Point out each Plasmodium parasite.
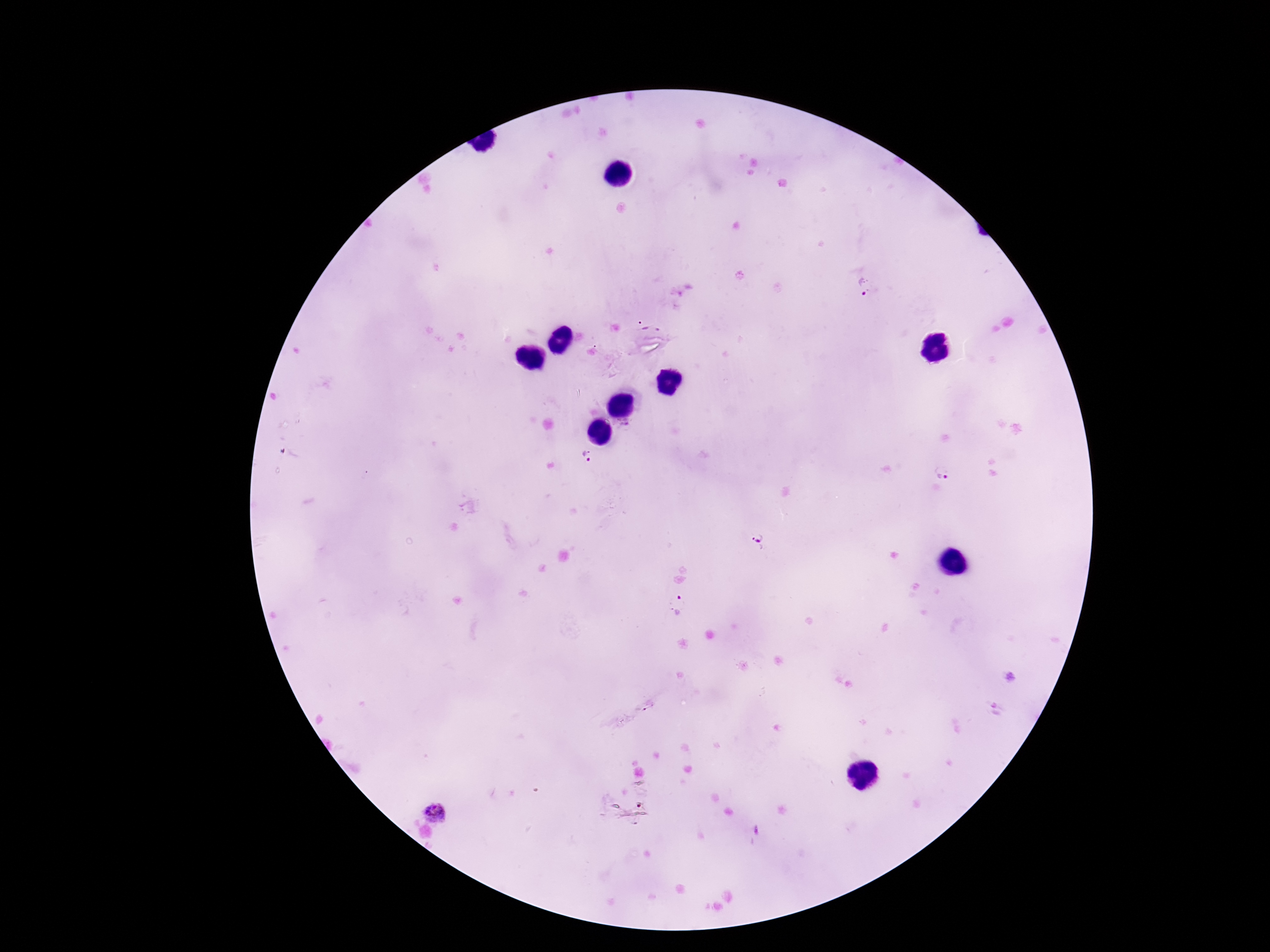

Approximate object centers, in pixels from the top-left corner.
Plasmodium parasites: (x=864, y=288), (x=587, y=455), (x=943, y=472), (x=759, y=541), (x=677, y=605), (x=436, y=810).

{
  "capture": "smartphone camera through the microscope eyepiece",
  "image_size": "1270×952 pixels",
  "preparation": "thick blood smear",
  "magnification": "100x",
  "field_of_view": "one from this slide",
  "patient_malaria_status": "infected",
  "stain": "Giemsa"
}